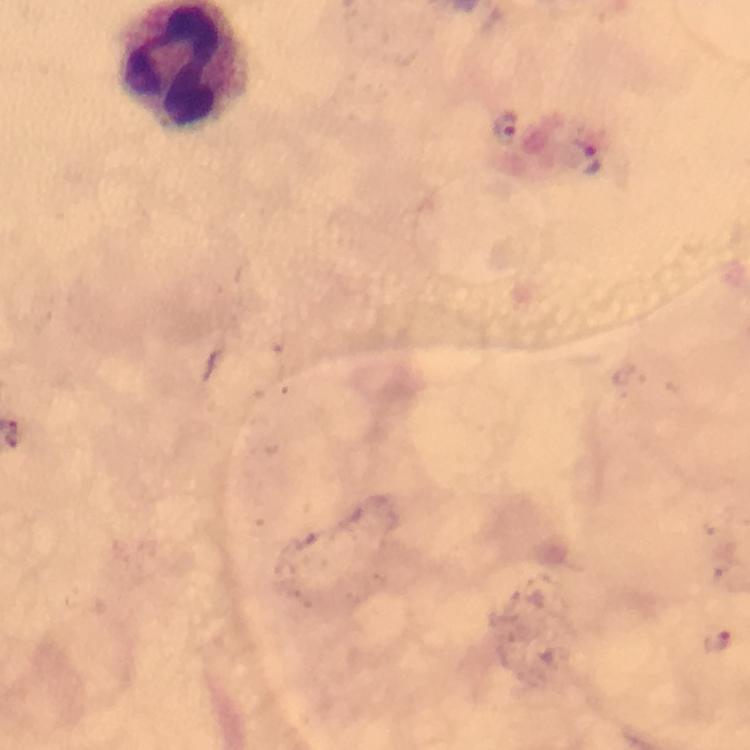

Approximate object centers, in pixels from the top-left corner. Malaria parasite locations: (x=508, y=128), (x=593, y=160), (x=718, y=639). Smartphone photograph taken through a microscope. Immersion oil applied. From a diagnostic examination for malaria. Giemsa-stained preparation. Thick smear. Image is 750×750 pixels. At 100x magnification. A crop from one field of view.